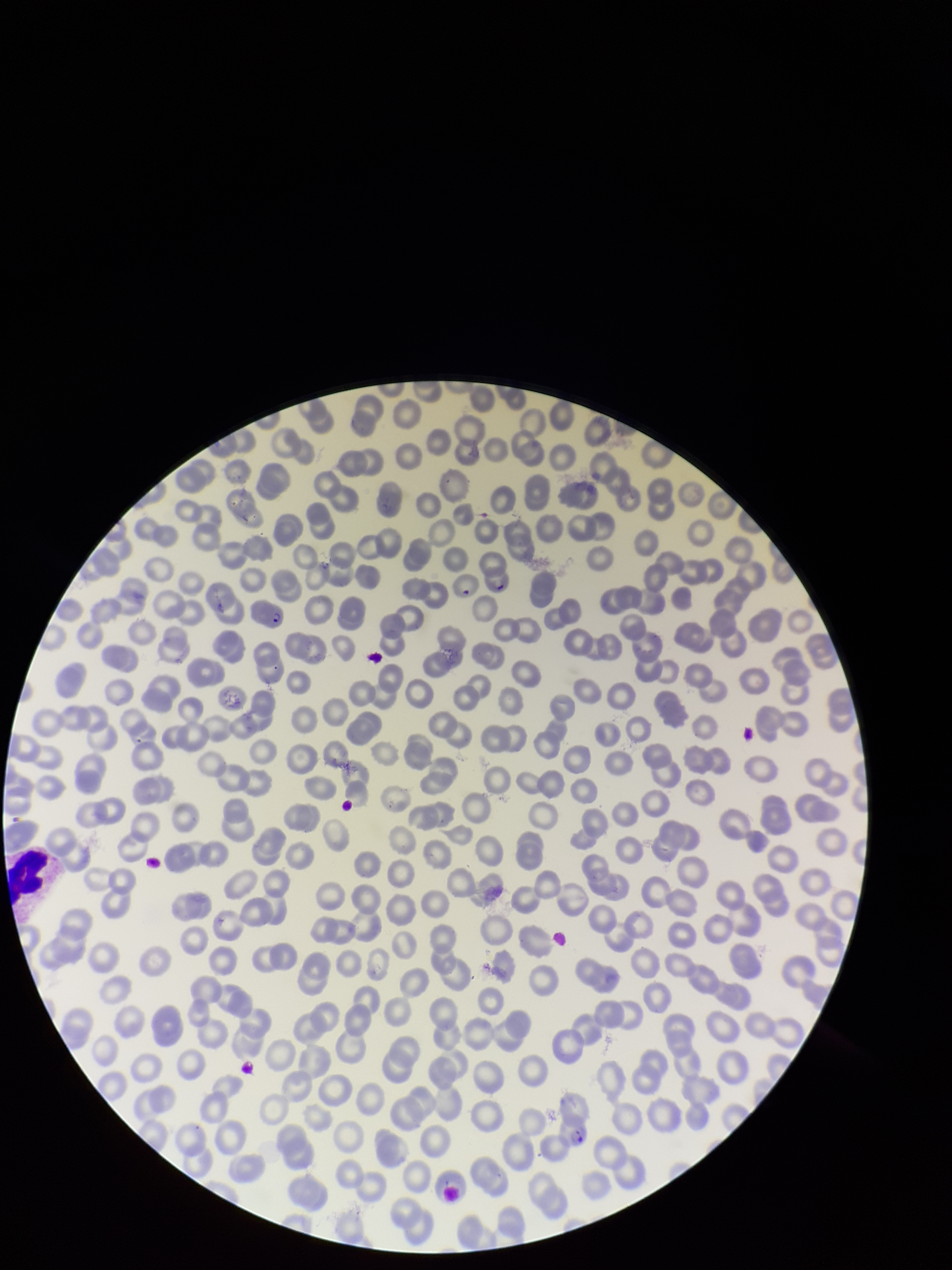 Species reported for this patient: Plasmodium falciparum. One field from this slide. Giemsa stain. Parasitized red blood cell count: 2. Image is 952×1270 pixels. Parasitized red blood cells: seen. Preparation: thin. Photographed through the microscope eyepiece with a smartphone camera. Red blood cell count: 260. Patient malaria status: positive.